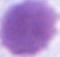
1000x magnification. An erythrocyte is seen. Photomicrograph.